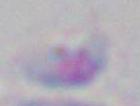 Toxoplasma gondii is seen. Micrograph. 1000x magnification.